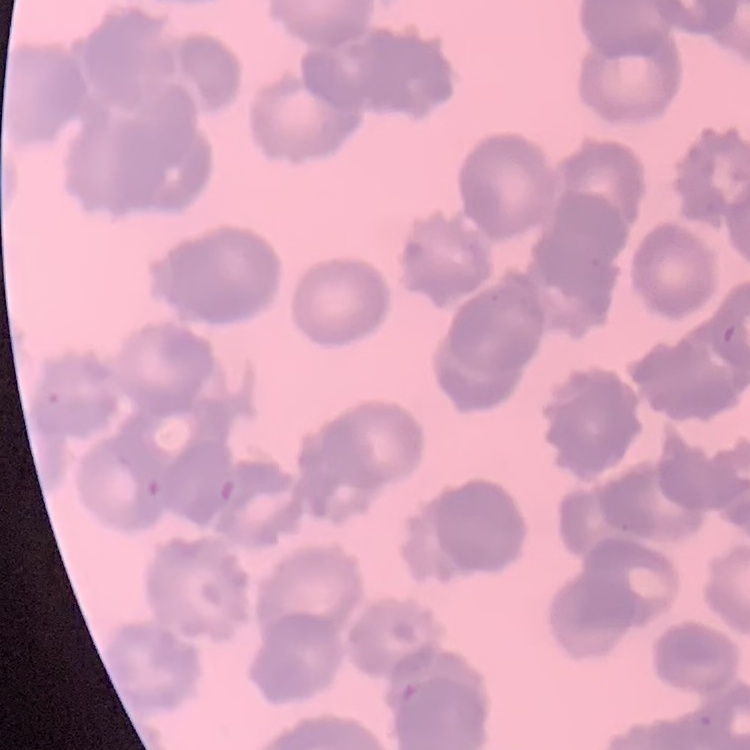

red blood cell morphology = rouleaux formation
preparation = thin peripheral smear
image type = one tile cut from a larger photomicrograph
stain = Field's or Giemsa